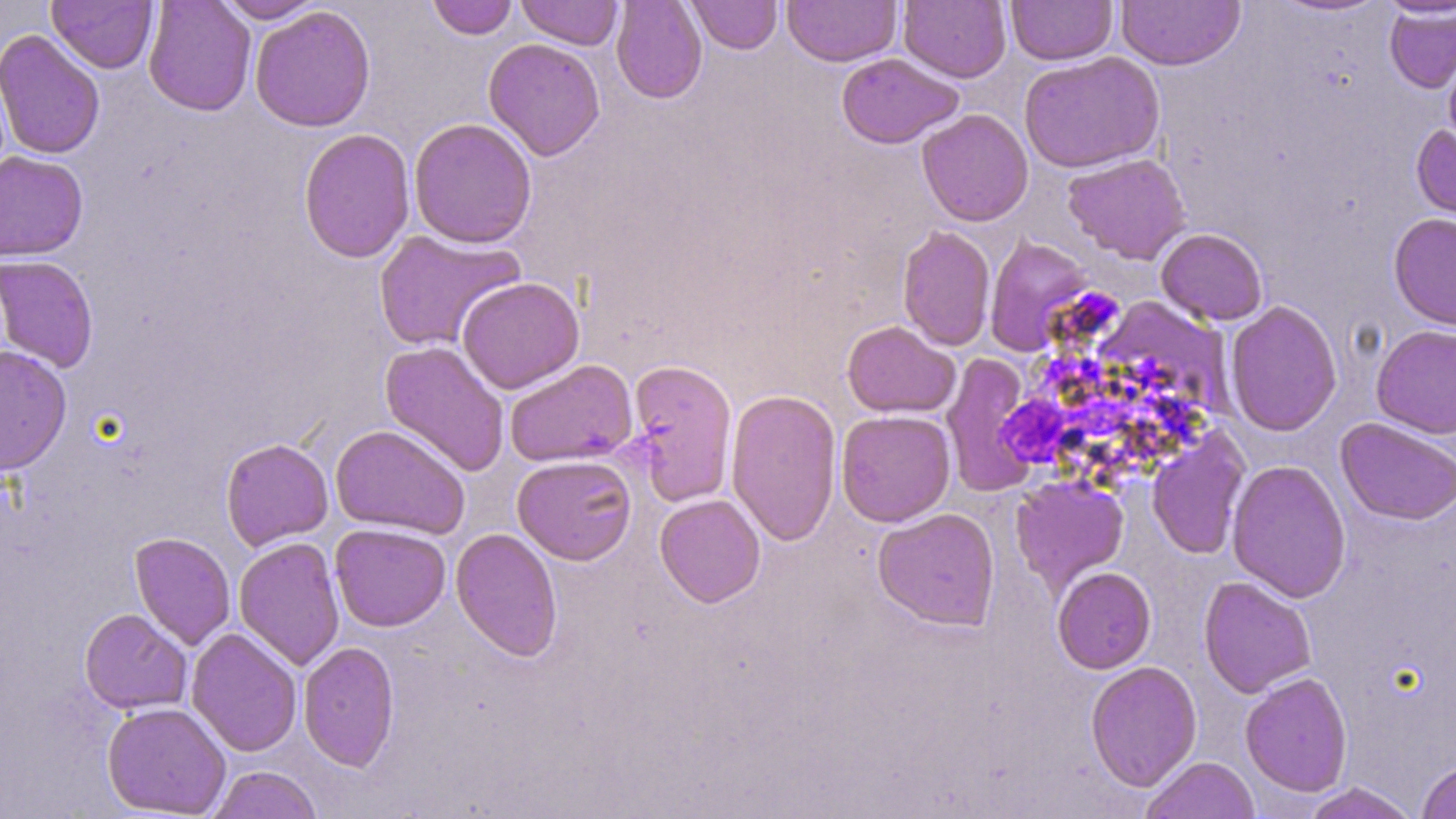
Summary:
  - Coordinate format: approximate bounding boxes as (x1, y1, x2, y2) in pixels
  - Uninfected red blood cell locations: (47, 0, 158, 73), (143, 0, 256, 116), (214, 0, 324, 23), (427, 0, 518, 40), (515, 0, 623, 50), (611, 0, 707, 104), (686, 0, 782, 55), (782, 0, 902, 67), (899, 0, 1011, 83), (1006, 0, 1117, 66), (1117, 0, 1246, 70), (1270, 0, 1393, 17), (1378, 0, 1456, 18), (1384, 3, 1456, 93), (250, 6, 376, 132), (0, 29, 105, 159), (483, 38, 606, 161), (1442, 41, 1456, 157), (1019, 50, 1165, 173), (836, 53, 964, 149), (917, 108, 1033, 226), (408, 117, 538, 248), (1411, 122, 1455, 241), (298, 128, 416, 263), (0, 150, 88, 261), (1062, 153, 1191, 264), (1388, 212, 1456, 330), (897, 225, 996, 351), (1156, 228, 1268, 326), (372, 229, 524, 352), (984, 235, 1094, 356), (0, 255, 99, 373), (457, 276, 584, 394), (1093, 296, 1231, 422), (1224, 299, 1342, 437), (842, 320, 960, 418), (1371, 324, 1456, 438), (379, 340, 510, 477), (0, 345, 72, 475), (942, 353, 1039, 497), (626, 357, 738, 506), (504, 359, 638, 467), (726, 388, 843, 547), (836, 409, 956, 527), (1336, 418, 1456, 525), (330, 424, 470, 539), (1147, 429, 1251, 560), (220, 437, 333, 550), (512, 455, 637, 565), (1226, 459, 1351, 603), (1011, 475, 1129, 593), (655, 494, 766, 608), (873, 507, 1000, 630), (330, 523, 450, 632), (450, 528, 563, 662), (129, 532, 236, 650), (234, 536, 345, 671), (1052, 566, 1156, 674), (1198, 576, 1317, 698), (79, 608, 191, 714), (186, 628, 302, 757), (298, 641, 400, 770), (1085, 660, 1202, 791), (1240, 671, 1353, 796), (101, 702, 231, 818), (1140, 756, 1260, 819), (1417, 760, 1456, 819), (206, 765, 324, 819), (1300, 782, 1421, 819)
  - Slide-level diagnosis: Plasmodium falciparum
  - Magnification: 1000x
  - Field of view: single
  - Image size: 1456×819 pixels
  - Modality: optical microscopy
  - Stain: May-Grünwald-Giemsa
  - Preparation: thin blood smear